Report the malaria status of this cell.
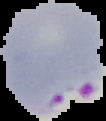

It is parasitized.

Summary:
  - Preparation: thin blood smear
  - Image type: segmented cell region with the area outside set to black
  - Image size: 106×121 pixels